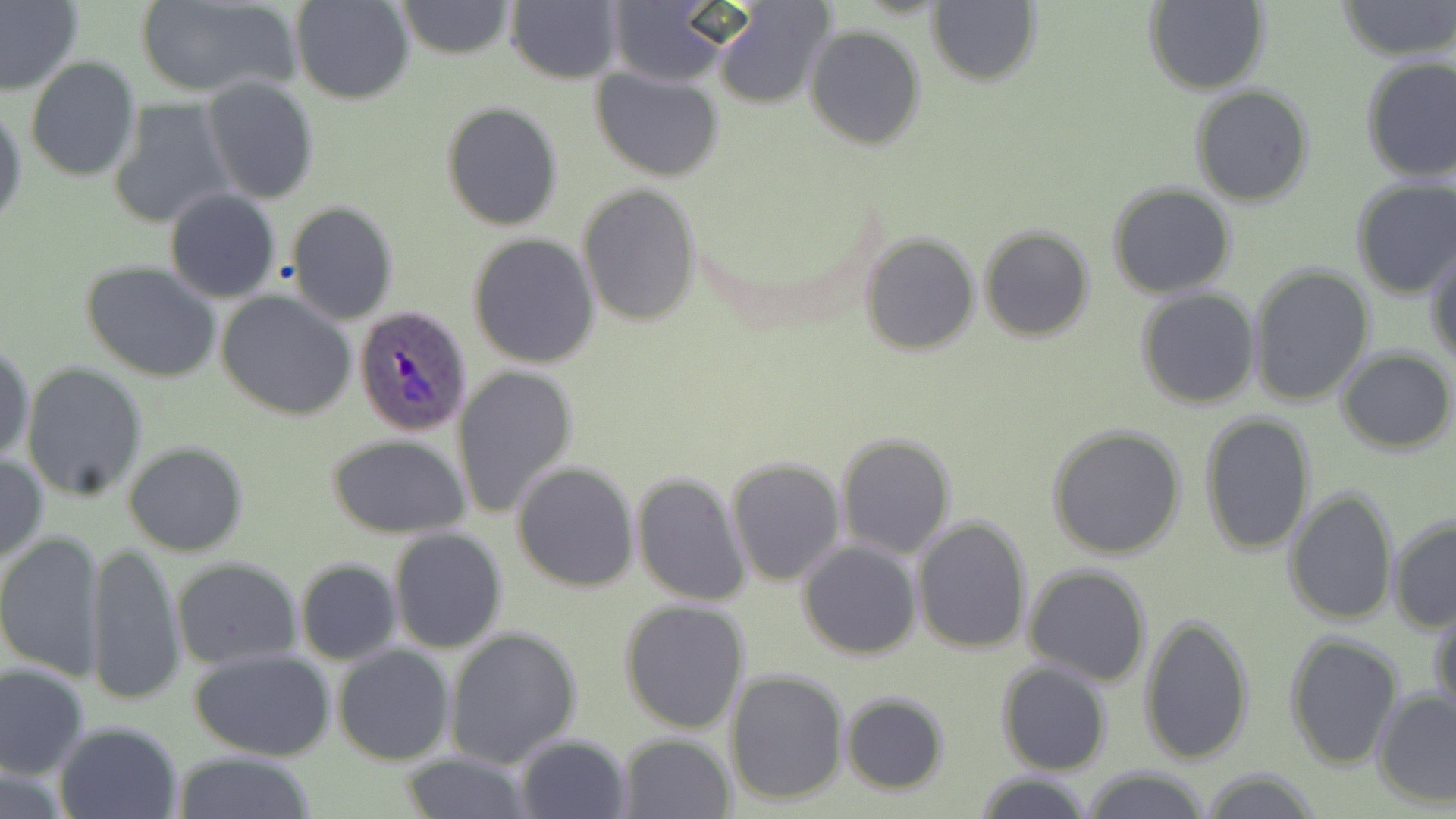

slide-level diagnosis = Plasmodium ovale
field of view = single
magnification = 1000x
preparation = thin blood film
Plasmodium ovale-infected red blood cell locations = approximate bounding boxes as named x1/y1/x2/y2 corners in pixels: (x1=355, y1=306, x2=473, y2=435)
modality = light microscopy
uninfected red blood cell locations = approximate bounding boxes as named x1/y1/x2/y2 corners in pixels: (x1=0, y1=0, x2=84, y2=99), (x1=290, y1=0, x2=414, y2=105), (x1=399, y1=0, x2=514, y2=59), (x1=1336, y1=0, x2=1455, y2=60), (x1=133, y1=1, x2=299, y2=99), (x1=927, y1=1, x2=1041, y2=88), (x1=1143, y1=1, x2=1269, y2=94), (x1=505, y1=2, x2=623, y2=84), (x1=605, y1=4, x2=733, y2=86), (x1=713, y1=4, x2=833, y2=108), (x1=804, y1=25, x2=927, y2=149), (x1=25, y1=56, x2=141, y2=183), (x1=1359, y1=57, x2=1456, y2=185), (x1=592, y1=67, x2=725, y2=181), (x1=202, y1=76, x2=319, y2=205), (x1=1191, y1=85, x2=1314, y2=207), (x1=110, y1=101, x2=234, y2=230), (x1=1, y1=102, x2=26, y2=229), (x1=441, y1=102, x2=563, y2=230), (x1=1350, y1=178, x2=1456, y2=300), (x1=1118, y1=181, x2=1248, y2=410), (x1=578, y1=184, x2=703, y2=326), (x1=1107, y1=184, x2=1237, y2=297), (x1=164, y1=190, x2=282, y2=303), (x1=287, y1=202, x2=398, y2=324), (x1=980, y1=225, x2=1094, y2=342), (x1=467, y1=233, x2=599, y2=369), (x1=861, y1=233, x2=979, y2=354), (x1=1426, y1=246, x2=1456, y2=368), (x1=79, y1=261, x2=222, y2=385), (x1=1246, y1=264, x2=1375, y2=407), (x1=1135, y1=290, x2=1259, y2=411), (x1=217, y1=291, x2=357, y2=420), (x1=0, y1=339, x2=34, y2=464), (x1=1337, y1=348, x2=1454, y2=454), (x1=21, y1=363, x2=148, y2=502), (x1=453, y1=364, x2=580, y2=518), (x1=1198, y1=411, x2=1317, y2=555), (x1=1046, y1=424, x2=1189, y2=560), (x1=326, y1=433, x2=473, y2=538), (x1=835, y1=433, x2=956, y2=559), (x1=122, y1=441, x2=248, y2=556), (x1=0, y1=452, x2=47, y2=565), (x1=726, y1=457, x2=846, y2=585), (x1=512, y1=461, x2=640, y2=591), (x1=631, y1=471, x2=751, y2=607), (x1=1284, y1=487, x2=1397, y2=627), (x1=911, y1=515, x2=1033, y2=655), (x1=1387, y1=515, x2=1456, y2=633), (x1=387, y1=527, x2=508, y2=654), (x1=0, y1=531, x2=105, y2=681), (x1=87, y1=539, x2=184, y2=708), (x1=798, y1=540, x2=923, y2=659), (x1=172, y1=558, x2=301, y2=669), (x1=294, y1=558, x2=401, y2=665), (x1=1024, y1=563, x2=1151, y2=685), (x1=618, y1=600, x2=751, y2=734), (x1=1432, y1=604, x2=1455, y2=721), (x1=1138, y1=613, x2=1255, y2=767), (x1=443, y1=626, x2=582, y2=768), (x1=1283, y1=632, x2=1402, y2=769), (x1=333, y1=646, x2=455, y2=766), (x1=187, y1=648, x2=340, y2=763), (x1=996, y1=662, x2=1112, y2=776), (x1=0, y1=663, x2=91, y2=780), (x1=726, y1=670, x2=850, y2=805), (x1=1372, y1=688, x2=1456, y2=807), (x1=840, y1=693, x2=950, y2=794), (x1=53, y1=721, x2=185, y2=819), (x1=617, y1=733, x2=736, y2=817), (x1=513, y1=734, x2=632, y2=819), (x1=174, y1=753, x2=320, y2=818), (x1=397, y1=754, x2=534, y2=817), (x1=0, y1=764, x2=74, y2=819), (x1=1081, y1=766, x2=1212, y2=819), (x1=1198, y1=769, x2=1322, y2=819), (x1=973, y1=772, x2=1096, y2=819)
stain = May-Grünwald-Giemsa
image size = 1456×819 pixels